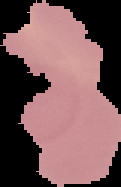

image_type: segmented cell region with the area outside set to black
preparation: thin blood film
image_size: 121×187 pixels
result: no Plasmodium parasites detected